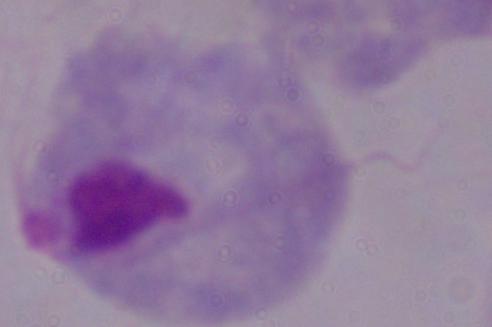

Summary:
  - Identification: trichomonad
  - Magnification: 1000x
  - Modality: photomicrograph